Name the parasite shown.
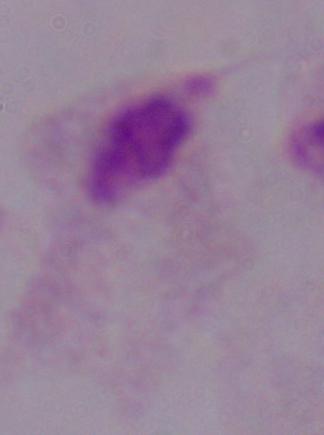

This is a trichomonad.

magnification = 1000x
modality = photomicrograph